Name the parasite shown.
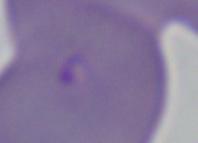
This is Babesia.

{
  "magnification": "1000x",
  "modality": "photomicrograph"
}